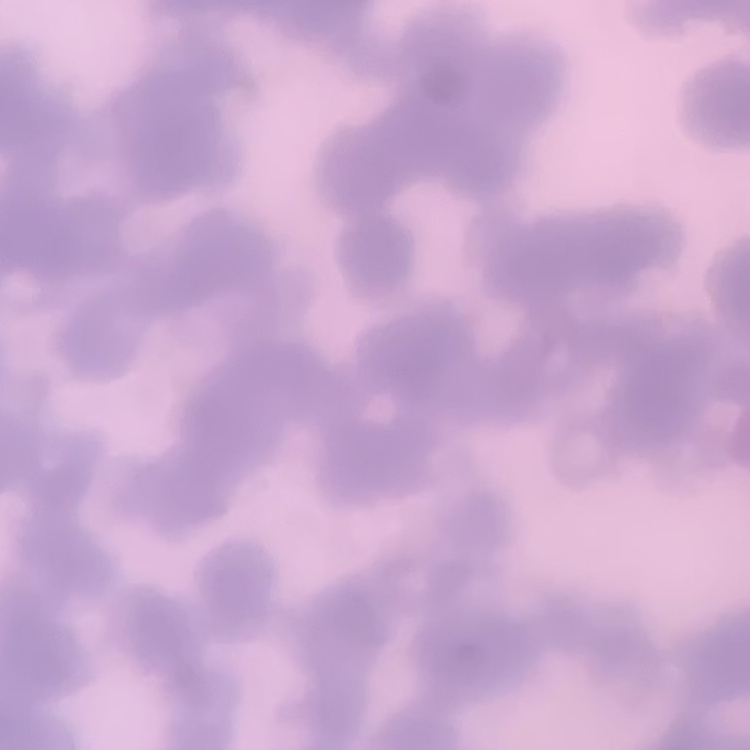
erythrocyte_morphology: rouleaux formation
stain: Field's or Giemsa
image_type: square crop of a larger photomicrograph
preparation: thin blood film